Describe the morphology of the erythrocytes.
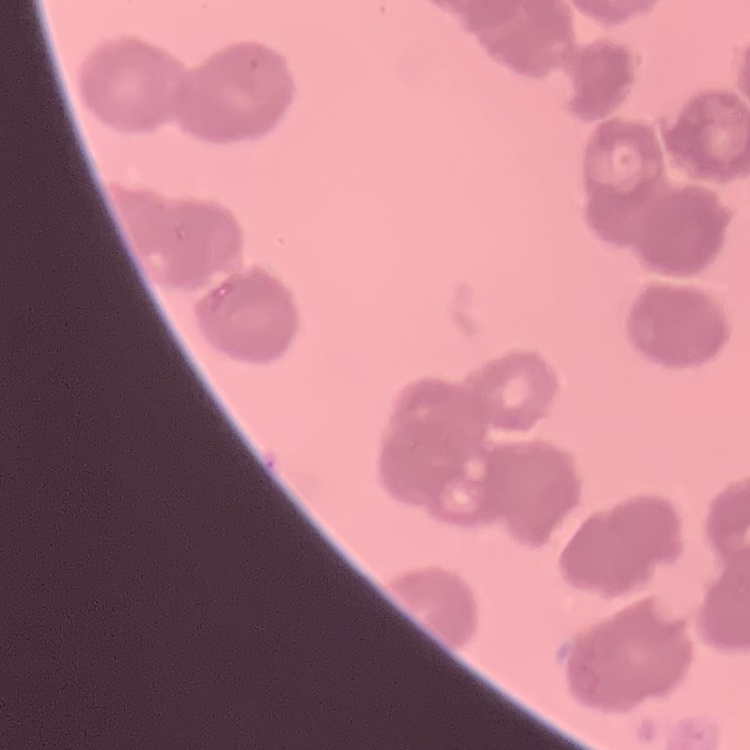

They show rouleaux formation.

Summary:
  - Image type: square crop of a larger photomicrograph
  - Preparation: thin peripheral smear
  - Stain: Field's or Giemsa